Describe the morphology of the erythrocytes.
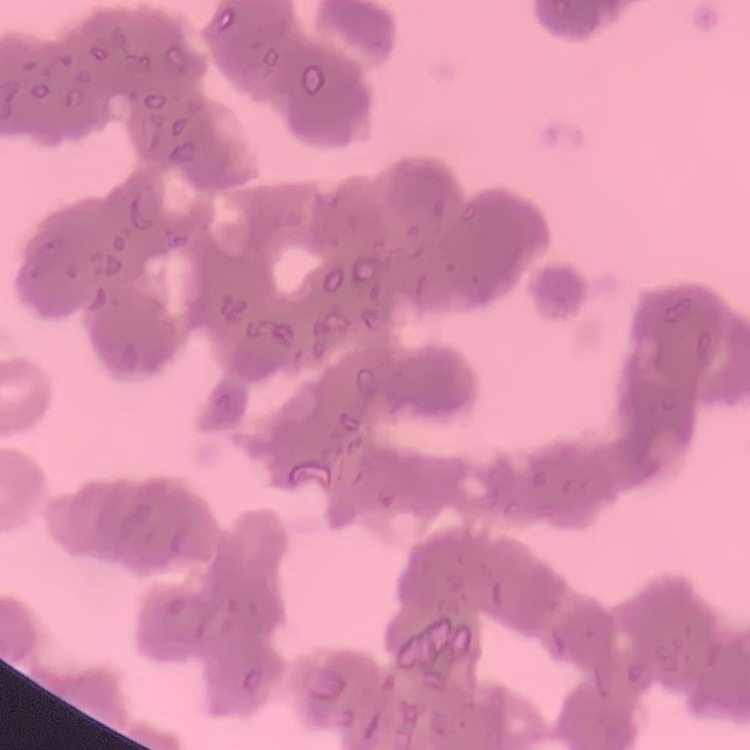

Rouleaux formation.

Thin blood smear. Field's or Giemsa stain. Square crop of a larger photomicrograph.